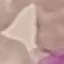
Result: no malaria parasites seen. Giemsa-stained preparation. Photographed with a smartphone camera at the microscope eyepiece. Automatically extracted cell patch, resized to 64 × 64 pixels. Thin smear of blood.